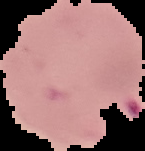

image size = 145×151 pixels
image type = cell region segmented out of the field of view; surrounding area masked to black
malaria status = parasitized
preparation = thin blood smear